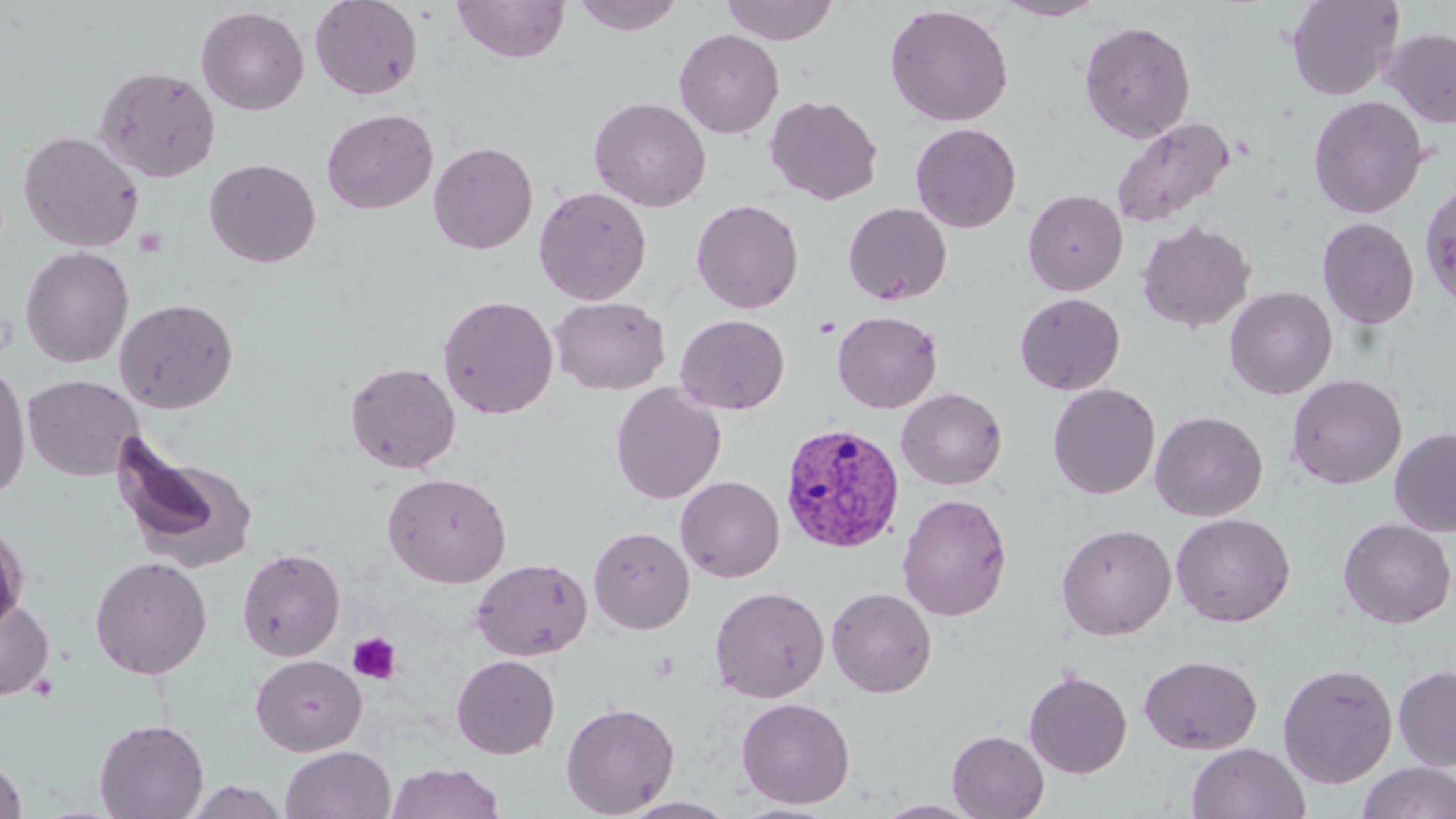
Approximate bounding boxes as [x1, y1, x2, y2] in pixels. Platelet locations: [135, 227, 168, 256], [348, 632, 402, 684]. Plasmodium vivax-infected red blood cell locations: [779, 423, 906, 554]. Uninfected red blood cell locations: [309, 0, 424, 100], [570, 0, 686, 35], [720, 0, 839, 45], [992, 0, 1106, 20], [1286, 0, 1405, 101], [453, 1, 571, 63], [884, 4, 1014, 127], [196, 5, 310, 115], [1079, 20, 1196, 142], [674, 28, 785, 139], [1382, 28, 1456, 128], [93, 64, 221, 182], [765, 94, 884, 205], [1308, 94, 1429, 219], [589, 96, 711, 212], [321, 108, 438, 215], [1111, 116, 1235, 229], [910, 122, 1022, 233], [18, 130, 145, 252], [428, 141, 539, 254], [204, 157, 321, 268], [1419, 179, 1456, 311], [534, 186, 652, 305], [1023, 189, 1128, 296], [691, 198, 804, 314], [843, 202, 952, 305], [1317, 217, 1421, 330], [1136, 220, 1255, 333], [21, 245, 134, 368], [1224, 286, 1337, 399], [1015, 292, 1126, 395], [437, 294, 559, 419], [550, 296, 671, 395], [114, 298, 239, 413], [832, 310, 943, 413], [675, 314, 790, 415], [345, 361, 462, 473], [0, 364, 32, 501], [1286, 373, 1408, 489], [23, 374, 143, 481], [610, 382, 726, 504], [1047, 382, 1161, 499], [896, 387, 1008, 491], [1150, 410, 1268, 522], [1389, 426, 1456, 537], [113, 440, 257, 571], [383, 472, 512, 588], [676, 476, 785, 583], [897, 493, 1012, 621], [1171, 512, 1296, 627], [1337, 518, 1456, 628], [0, 521, 29, 640], [1055, 522, 1177, 639], [588, 526, 695, 634], [237, 548, 345, 661], [90, 556, 213, 679], [471, 558, 592, 660], [709, 586, 830, 702], [826, 587, 937, 697], [0, 595, 55, 701], [250, 654, 367, 756], [451, 654, 560, 759], [1139, 655, 1262, 755], [1277, 662, 1398, 788], [1393, 665, 1456, 772], [1023, 669, 1132, 779], [736, 697, 855, 809], [561, 701, 680, 817], [94, 718, 209, 819], [947, 729, 1049, 818], [1187, 742, 1310, 819], [281, 745, 396, 819], [0, 757, 28, 819], [385, 762, 505, 819], [1357, 762, 1456, 819], [182, 780, 290, 819], [620, 796, 739, 818], [872, 800, 985, 818], [731, 801, 844, 818]. Slide-level diagnosis: Plasmodium vivax. One field of a larger specimen. Image is 1456×819 pixels. Thin blood smear. Captured at 1000x magnification. May-Grünwald-Giemsa stain. Light microscopy.